Locate the cells, classifying each as a parasitized red blood cell, an uninfected red blood cell, or a white blood cell.
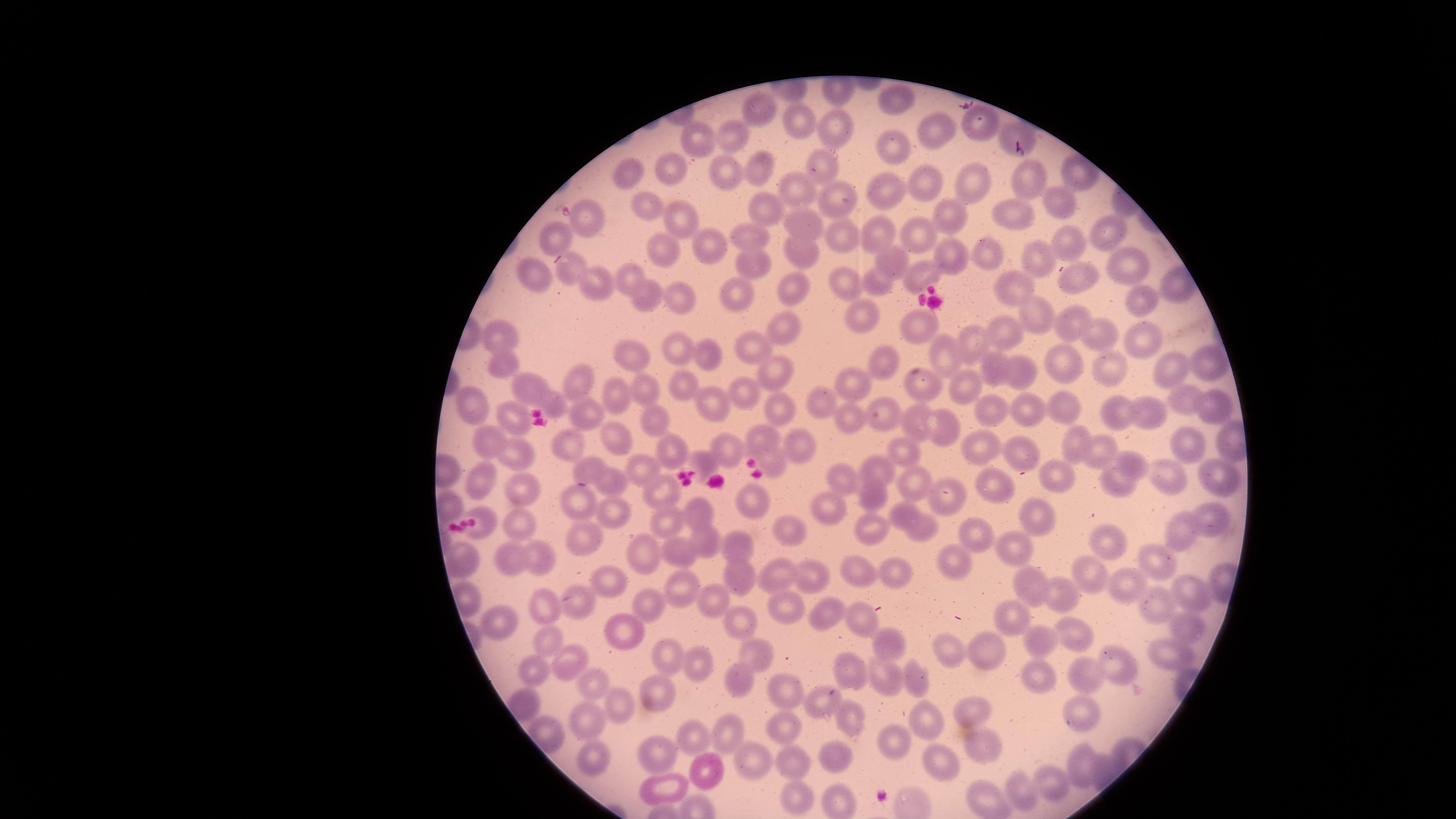

No parasitized red blood cells identified.
Approximate marker points as [x, y] in pixels.
Uninfected red blood cells: [893, 100], [759, 114], [832, 119], [799, 123], [941, 129], [1010, 131], [730, 134], [699, 138], [893, 144], [818, 160], [668, 169], [764, 169], [630, 171], [725, 171], [1034, 176], [922, 181], [976, 183], [885, 191], [801, 192], [837, 197], [1065, 201], [646, 206], [764, 210], [1011, 210], [683, 215], [587, 218], [949, 218], [803, 227], [554, 231], [877, 231], [837, 232], [1111, 232], [754, 235], [920, 235], [1067, 239], [708, 240], [664, 248], [797, 249], [951, 249], [993, 252], [889, 256], [1040, 258], [755, 261], [1130, 268], [529, 269], [568, 270], [1081, 272], [627, 274], [918, 275], [847, 277], [602, 281], [875, 281], [1018, 289], [792, 293], [670, 294], [646, 297], [740, 298], [1142, 302], [865, 313], [1034, 317], [1071, 321], [782, 326], [926, 328], [1013, 333], [1146, 333], [1097, 334], [497, 336], [972, 338], [755, 344], [675, 347], [706, 351], [955, 352], [632, 355], [882, 361], [497, 362], [1055, 363], [1001, 365], [775, 368], [1170, 368], [1203, 368], [1020, 371], [1111, 371], [579, 377], [849, 381], [972, 381], [526, 382], [922, 384], [645, 386], [685, 386], [739, 390], [621, 394], [819, 399], [552, 401], [1184, 401], [708, 402], [1208, 403], [469, 404], [780, 409], [1064, 409], [584, 410], [1033, 410], [1146, 412], [888, 414], [1121, 414], [656, 416], [850, 416], [985, 418], [518, 420], [916, 420], [933, 423], [484, 438], [622, 438], [761, 439], [1075, 439], [562, 444], [982, 445], [730, 446], [795, 447], [1187, 449], [672, 450], [1018, 450], [1103, 451], [903, 454], [513, 457], [704, 459], [778, 464], [1135, 464], [882, 465], [588, 466], [637, 468], [1217, 474], [1058, 475], [842, 478], [921, 478], [1170, 480], [478, 482], [517, 484], [995, 485], [1121, 485], [611, 486], [657, 488], [872, 490], [577, 497], [750, 498], [444, 504], [829, 508], [699, 511], [615, 512], [902, 513], [1216, 517], [1036, 519], [519, 521], [666, 522], [873, 523], [484, 525], [920, 528], [974, 529], [1189, 529], [584, 530], [785, 531], [703, 538], [1109, 540], [733, 547], [1010, 548], [674, 552], [647, 554], [465, 556], [537, 556], [1158, 558], [508, 560], [954, 564], [901, 567], [781, 571], [862, 573], [1087, 574], [612, 577], [738, 577], [814, 577], [1028, 582], [1122, 582], [684, 586], [1191, 589], [1062, 592], [714, 598], [1150, 601], [548, 602], [778, 602], [583, 604], [651, 606], [828, 613], [1010, 620], [1180, 621], [738, 622], [858, 623], [501, 624], [1073, 631], [544, 633], [629, 633], [1036, 641], [888, 644], [946, 644], [985, 648], [759, 650], [1177, 651], [661, 654], [697, 659], [569, 662], [1122, 666], [535, 668], [1081, 668], [855, 670], [916, 676], [1039, 676], [743, 681], [888, 681], [594, 682], [785, 688], [663, 693], [825, 702], [518, 703], [624, 708], [1073, 710], [968, 712], [853, 717], [925, 718], [591, 723], [785, 725], [726, 730], [690, 736], [891, 742], [990, 747], [832, 754], [665, 755], [591, 757], [752, 758], [793, 759], [941, 764], [1084, 768], [709, 775], [664, 784], [1054, 784], [1019, 793], [800, 798], [834, 798], [986, 800].
No white blood cells identified.

Summary:
  - Capture: smartphone photograph through the microscope eyepiece
  - Image size: 1456×819 pixels
  - Field of view: single
  - Preparation: thin blood smear
  - Stain: Giemsa
  - Visible region: circular